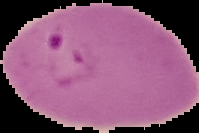

Summary:
  - Preparation: thin blood smear
  - Image size: 199×133 pixels
  - Malaria status: parasitized
  - Image type: segmented cell region on a black background